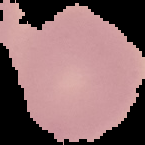 The area outside the segmented cell region is set to black. Image is 145×145 pixels. Malaria status: uninfected. From a thin blood film.